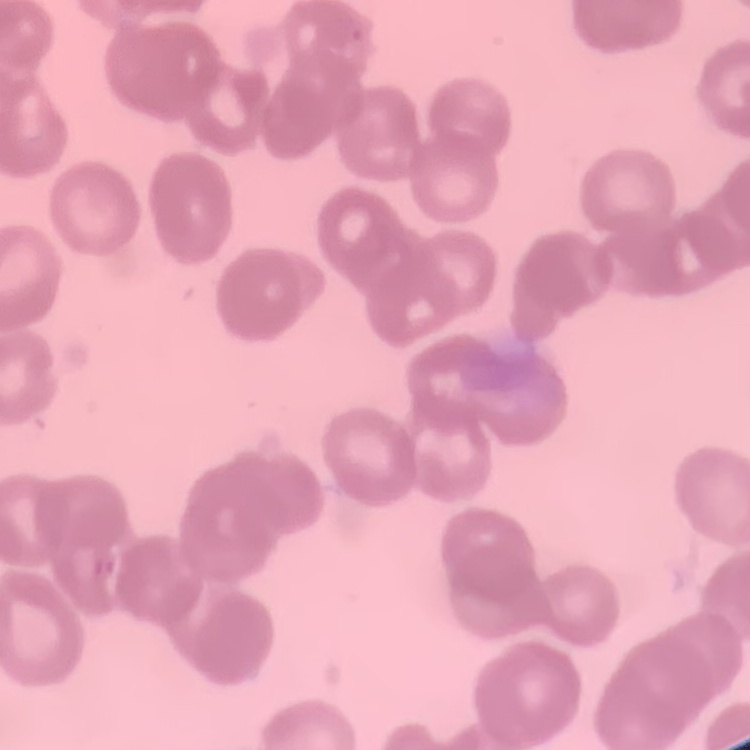

The erythrocytes show rouleaux formation. One tile cut from a larger photomicrograph. Field's or Giemsa stain. Thin peripheral smear.